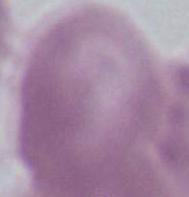

Summary:
  - Magnification: 1000x
  - Modality: photomicrograph
  - Identification: erythrocyte